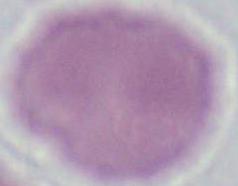
Captured at 1000x magnification. An erythrocyte is seen. Photomicrograph.